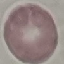
Summary:
  - Result: negative for malaria parasites
  - Image type: cell patch, automatically extracted from a larger field of view and resized to 64 × 64 pixels
  - Stain: Giemsa
  - Preparation: thin blood smear
  - Capture: smartphone camera at the microscope eyepiece